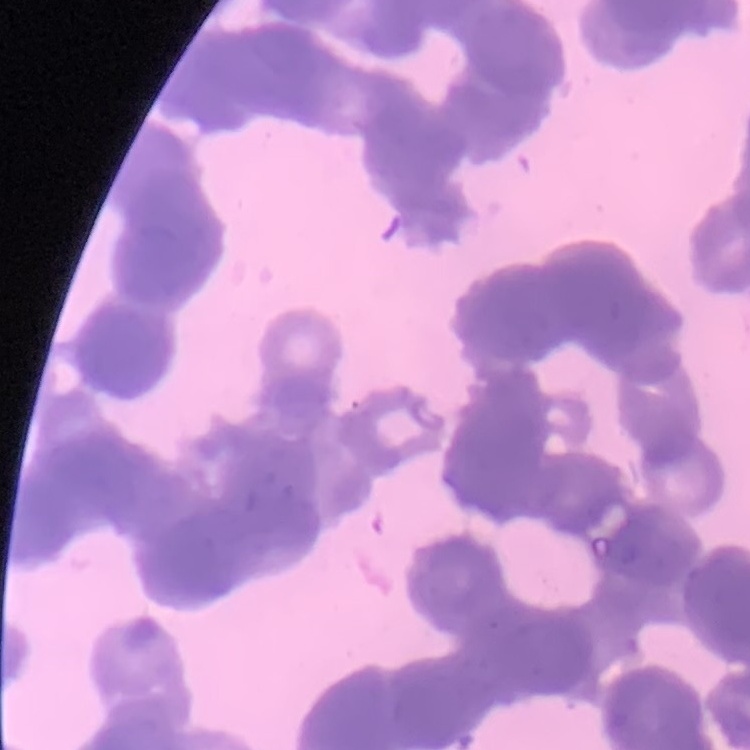

red blood cell morphology = rouleaux formation
stain = Field's or Giemsa
preparation = thin peripheral smear
image type = square crop of a larger photomicrograph